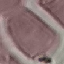 Result: no malaria parasites detected. Acquired by smartphone through the microscope eyepiece. Cell patch, automatically extracted from a larger field of view and resized to 64 × 64 pixels. Thin smear of blood. Giemsa stain.